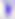

Toxoplasma gondii is seen. 400x magnification. Micrograph.